Report the malaria status of this cell.
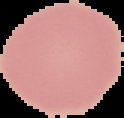

Uninfected.

From a thin blood film. The area outside the segmented cell region is set to black. Image is 124×118 pixels.